Identify the blood parasite species.
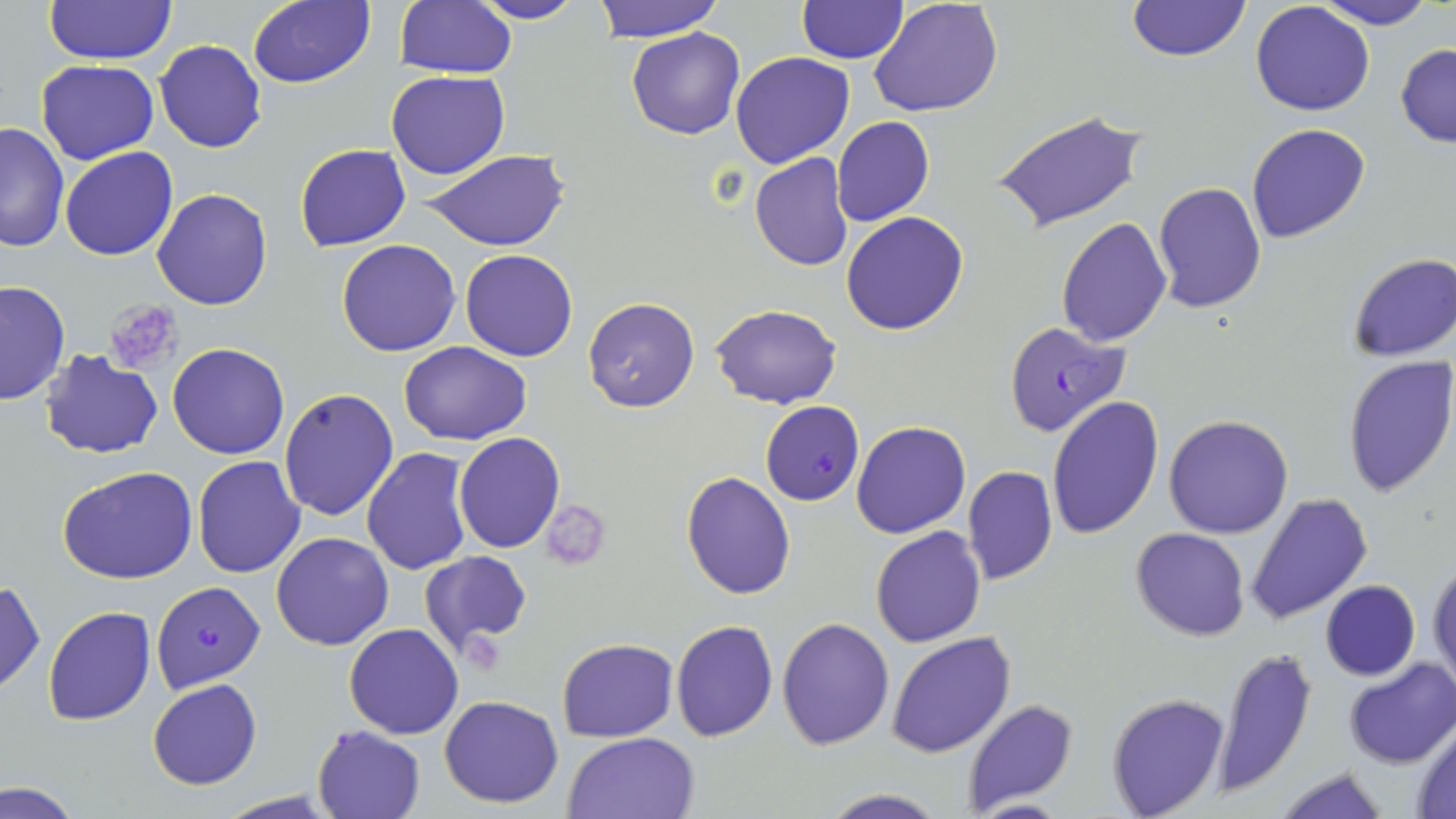

Plasmodium falciparum.

Summary:
  - Coordinate format: approximate bounding boxes as (x1,y1)-(x2,y2) corner pairs in pixels
  - Uninfected red blood cell locations: (44,0)-(177,65), (393,0)-(517,79), (468,0)-(590,24), (593,0)-(726,41), (869,0)-(1004,118), (1309,0)-(1441,29), (247,1)-(375,89), (797,1)-(908,64), (1127,1)-(1251,63), (1250,3)-(1375,117), (627,28)-(745,140), (154,39)-(268,154), (1395,43)-(1456,148), (730,51)-(855,168), (36,60)-(159,165), (386,68)-(510,179), (993,109)-(1147,233), (831,116)-(934,227), (0,121)-(70,252), (1245,123)-(1371,245), (295,143)-(410,251), (59,147)-(179,261), (423,150)-(568,250), (749,152)-(854,271), (1152,181)-(1267,315), (152,189)-(273,310), (842,211)-(967,335), (1055,218)-(1173,348), (334,240)-(461,357), (460,250)-(579,362), (1347,252)-(1456,362), (1,281)-(70,406), (583,297)-(698,413), (711,304)-(841,408), (399,342)-(532,446), (168,343)-(289,459), (40,350)-(163,458), (1341,355)-(1456,500), (278,388)-(398,522), (1045,396)-(1163,541), (1164,415)-(1293,539), (851,420)-(970,539), (455,432)-(565,552), (361,447)-(473,576), (192,455)-(306,577), (57,465)-(198,584), (963,466)-(1058,585), (682,471)-(795,598), (1245,492)-(1372,627), (540,499)-(611,570), (870,527)-(986,648), (1131,527)-(1251,642), (270,531)-(394,651), (420,551)-(533,658), (1427,559)-(1455,691), (0,579)-(44,694), (1320,580)-(1421,682), (43,606)-(157,727), (775,616)-(895,750), (670,618)-(777,741), (344,623)-(464,740), (887,630)-(1015,757), (556,638)-(677,742), (1212,649)-(1316,795), (1343,658)-(1455,769), (148,679)-(261,790), (1105,692)-(1231,818), (440,695)-(565,807), (960,698)-(1080,814), (1410,721)-(1456,817), (312,725)-(424,819), (562,731)-(699,818), (1271,764)-(1391,819), (2,779)-(85,818), (817,789)-(950,818), (213,791)-(344,819)
  - Platelet locations: (104,298)-(183,378)
  - Plasmodium falciparum-infected red blood cell locations: (1002,321)-(1132,437), (760,402)-(863,503), (151,582)-(265,691)
  - Preparation: thin blood smear
  - Magnification: 1000x
  - Image size: 1456×819 pixels
  - Stain: May-Grünwald-Giemsa
  - Modality: light microscopy
  - Field of view: one of a larger specimen